Assess the morphology of the red blood cells.
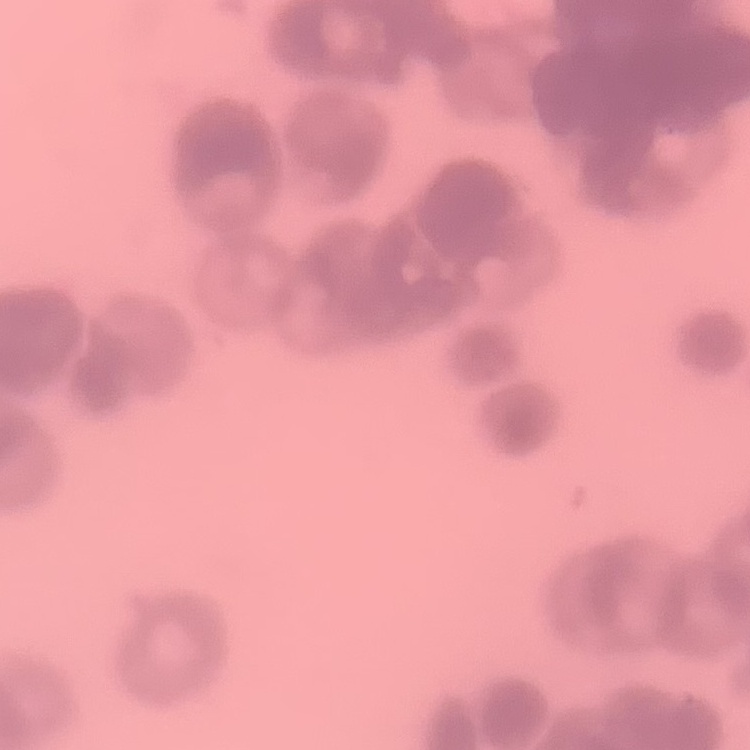
Rouleaux formation.

Summary:
  - Image type: one tile cut from a larger photomicrograph
  - Preparation: thin blood smear
  - Stain: Field's or Giemsa